Classify this cell by malaria status.
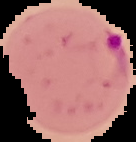
It is parasitized.

image size = 136×142 pixels
preparation = thin blood film
image type = segmented cell region with the area outside set to black